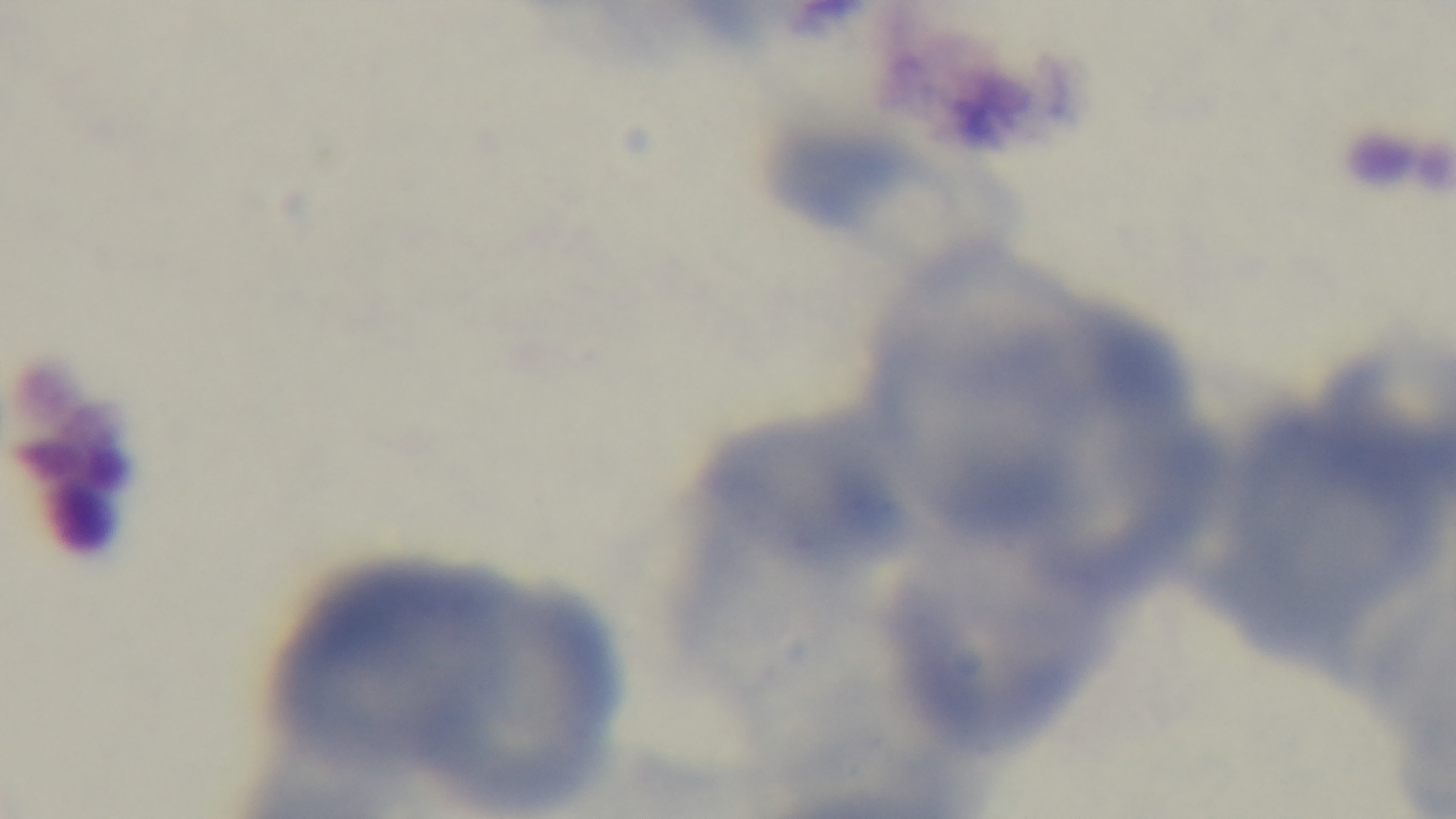
field of view = one from the slide
malaria status = negative
stain = Giemsa
modality = light microscopy
objective = 100x oil immersion
capture = mounted 4K digital camera
preparation = thin